Locate every blood parasite and identify its species.
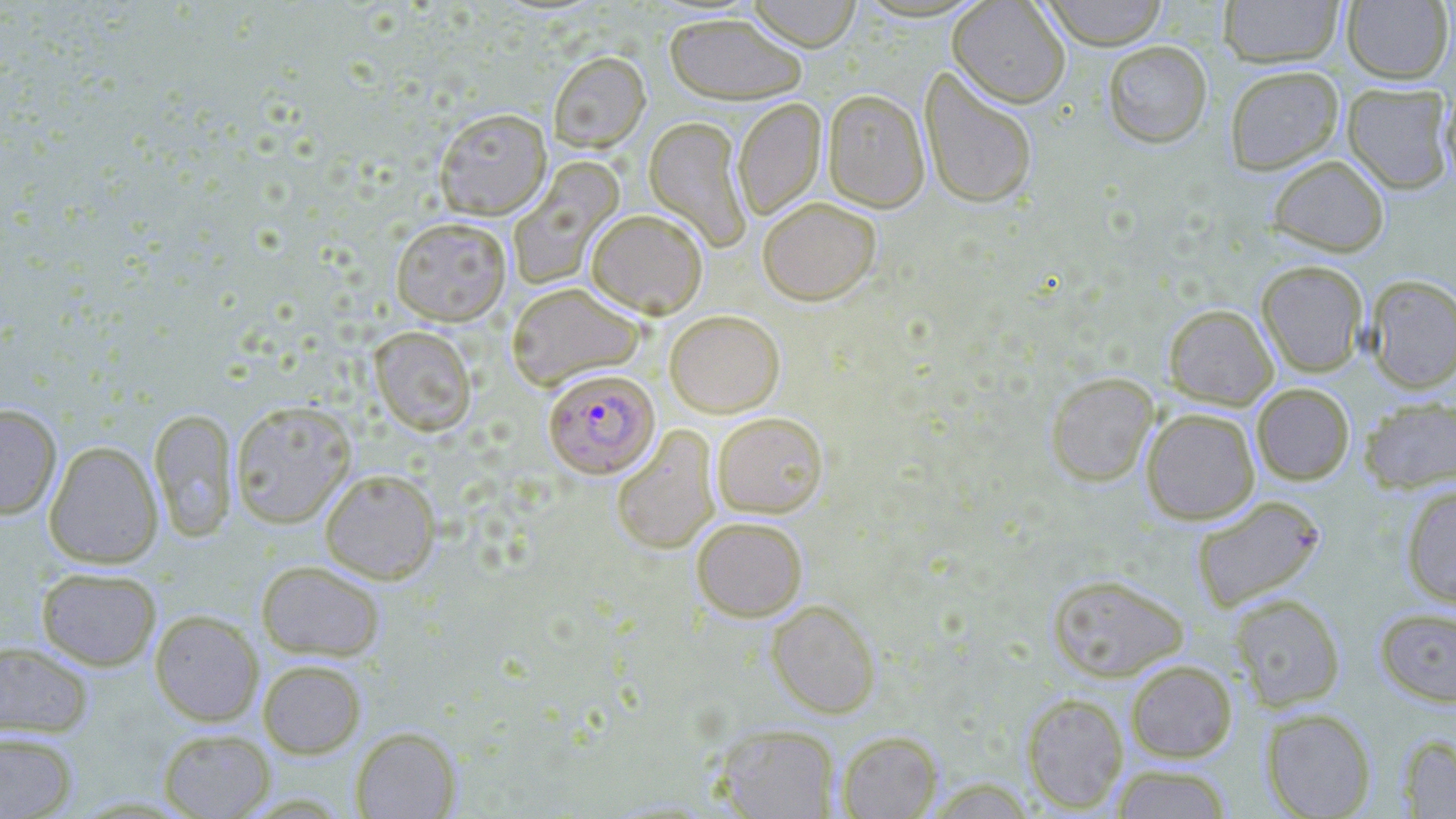

Approximate bounding boxes as named x1/y1/x2/y2 corners in pixels.
Plasmodium falciparum-infected red blood cells: (x1=543, y1=368, x2=659, y2=478).
No Plasmodium ovale, Plasmodium malariae, Plasmodium vivax, Babesia divergens, or Trypanosoma brucei observed.

{
  "slide_level_diagnosis": "Plasmodium falciparum",
  "field_of_view": "single",
  "stain": "May-Grünwald-Giemsa",
  "preparation": "thin blood smear",
  "modality": "optical microscopy",
  "uninfected_red_blood_cell_locations": "approximate bounding boxes as named x1/y1/x2/y2 corners in pixels: (x1=745, y1=0, x2=862, y2=51), (x1=947, y1=0, x2=1070, y2=107), (x1=1041, y1=0, x2=1168, y2=49), (x1=1218, y1=0, x2=1344, y2=68), (x1=1341, y1=1, x2=1454, y2=84), (x1=664, y1=12, x2=808, y2=104), (x1=1102, y1=41, x2=1212, y2=147), (x1=548, y1=51, x2=650, y2=153), (x1=1224, y1=65, x2=1344, y2=174), (x1=920, y1=67, x2=1038, y2=210), (x1=1342, y1=82, x2=1455, y2=194), (x1=1440, y1=87, x2=1456, y2=187), (x1=823, y1=88, x2=930, y2=213), (x1=733, y1=98, x2=826, y2=221), (x1=433, y1=107, x2=552, y2=220), (x1=644, y1=116, x2=752, y2=252), (x1=1268, y1=155, x2=1389, y2=257), (x1=507, y1=158, x2=625, y2=292), (x1=758, y1=196, x2=881, y2=306), (x1=586, y1=208, x2=708, y2=318), (x1=390, y1=216, x2=512, y2=325), (x1=1256, y1=260, x2=1368, y2=377), (x1=1365, y1=274, x2=1456, y2=393), (x1=506, y1=282, x2=646, y2=391), (x1=1164, y1=304, x2=1278, y2=409), (x1=664, y1=309, x2=785, y2=417), (x1=369, y1=325, x2=477, y2=435), (x1=1045, y1=371, x2=1159, y2=487), (x1=1252, y1=383, x2=1354, y2=485), (x1=1359, y1=396, x2=1455, y2=493), (x1=229, y1=399, x2=357, y2=528), (x1=0, y1=404, x2=61, y2=520), (x1=148, y1=407, x2=238, y2=542), (x1=1141, y1=408, x2=1260, y2=524), (x1=712, y1=411, x2=828, y2=517), (x1=611, y1=424, x2=721, y2=555), (x1=44, y1=441, x2=163, y2=568), (x1=319, y1=467, x2=441, y2=583), (x1=1400, y1=483, x2=1456, y2=608), (x1=1191, y1=494, x2=1326, y2=613), (x1=691, y1=516, x2=808, y2=621), (x1=256, y1=559, x2=386, y2=661), (x1=37, y1=567, x2=161, y2=670), (x1=1046, y1=573, x2=1189, y2=682), (x1=1229, y1=593, x2=1346, y2=710), (x1=766, y1=599, x2=881, y2=718), (x1=1374, y1=607, x2=1456, y2=707), (x1=150, y1=609, x2=263, y2=726), (x1=0, y1=640, x2=94, y2=739), (x1=258, y1=659, x2=367, y2=758), (x1=1125, y1=659, x2=1237, y2=762), (x1=1022, y1=692, x2=1128, y2=813), (x1=1261, y1=707, x2=1376, y2=819), (x1=716, y1=724, x2=841, y2=818), (x1=350, y1=726, x2=460, y2=818), (x1=158, y1=728, x2=275, y2=818), (x1=836, y1=730, x2=943, y2=818), (x1=0, y1=731, x2=78, y2=818), (x1=1397, y1=733, x2=1456, y2=817), (x1=1110, y1=764, x2=1234, y2=819)",
  "magnification": "1000x",
  "image_size": "1456×819 pixels"
}